Assess the morphology of the erythrocytes.
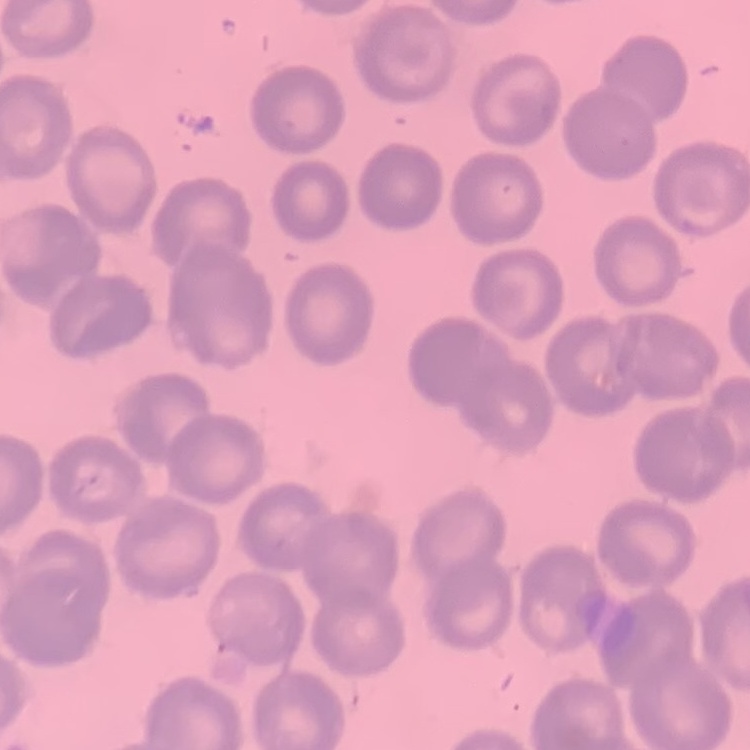
No rouleaux formation.

Summary:
  - Preparation: thin blood film
  - Stain: Field's or Giemsa
  - Image type: square crop of a larger photomicrograph